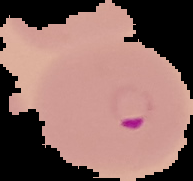
image size = 193×181 pixels
result = malaria parasites identified
image type = segmented cell region on a black background
preparation = thin blood smear